Describe the morphology of the red blood cells.
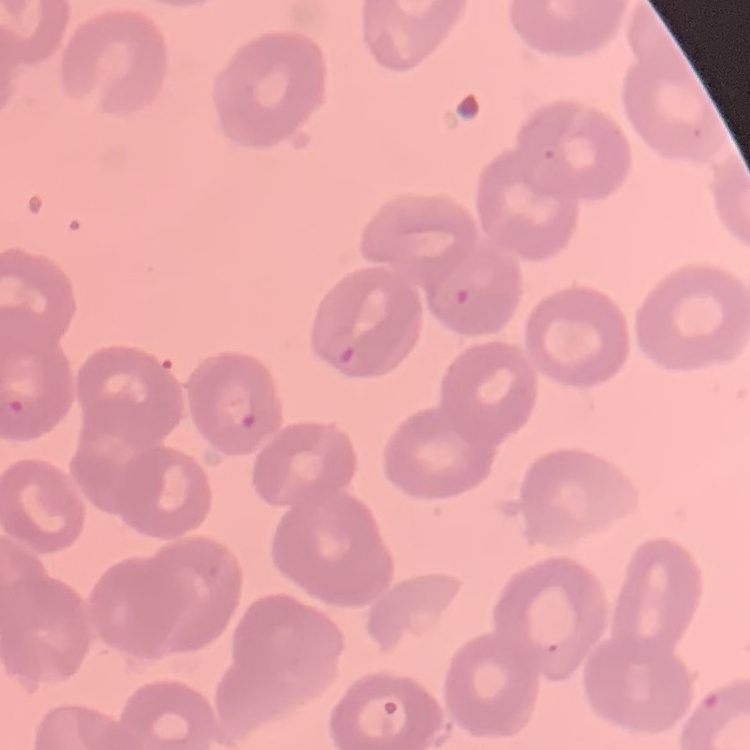
No rouleaux formation.

preparation = thin peripheral smear
image type = one tile cut from a larger photomicrograph
stain = Field's or Giemsa